Assess this cell for malaria.
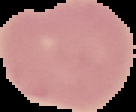

It is uninfected.

image size = 136×112 pixels
image type = segmented cell region with the area outside set to black
preparation = thin blood smear